Identify the parasite.
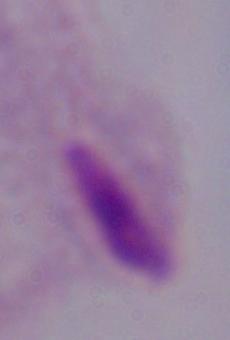
A trichomonad.

Captured at 1000x magnification. Photomicrograph.